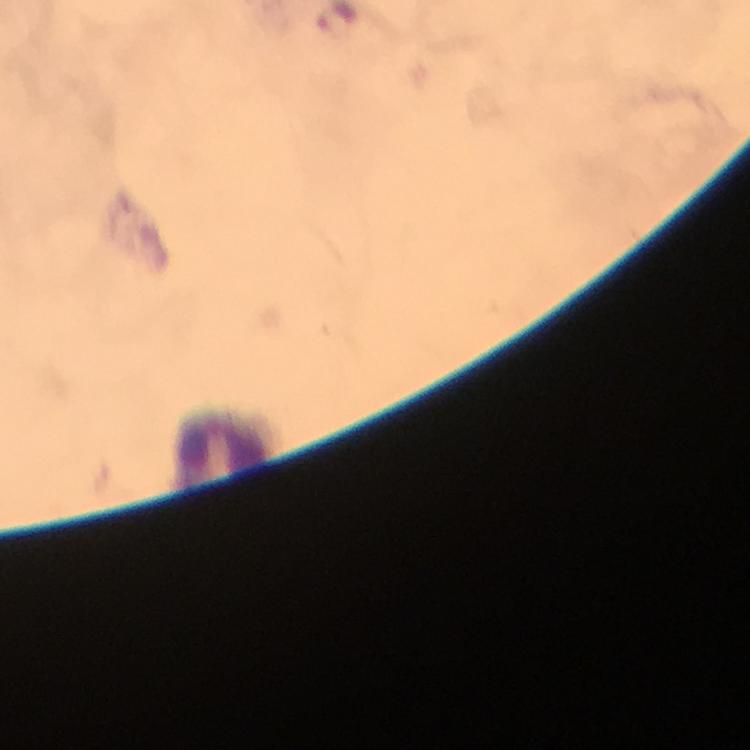
image size = 750×750 pixels
immersion oil = applied
cropped from = one field of view
context = from a malaria diagnostic workup
leukocyte locations = approximate centers as {x, y} in pixels: {224, 450}
malaria parasites = none seen
stain = Giemsa
magnification = 100x
capture = smartphone mounted on the microscope
preparation = thick blood film